Name the cell type shown.
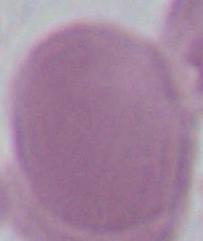

This is an erythrocyte.

magnification = 1000x
modality = micrograph